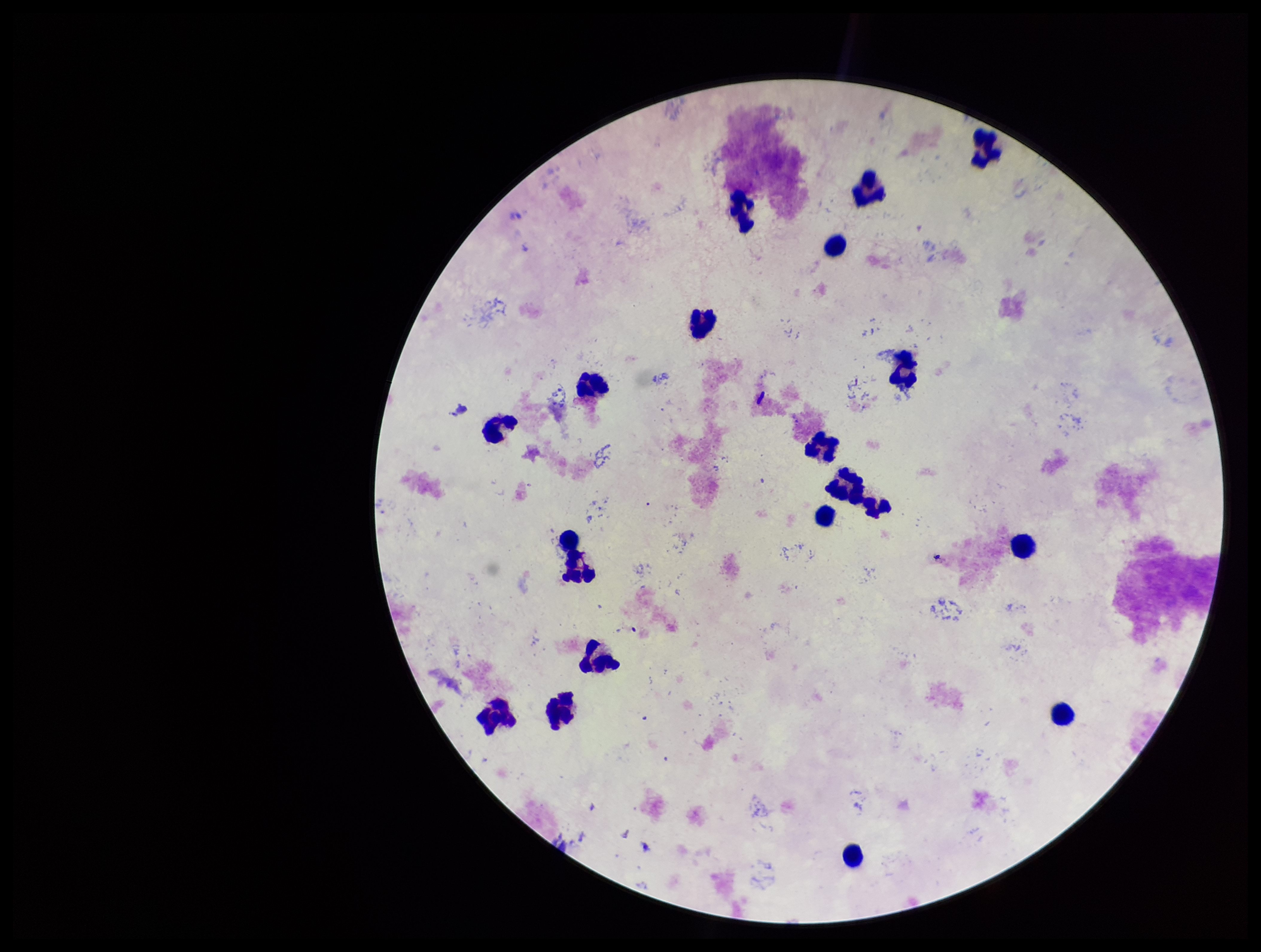 Patient malaria status: negative. Giemsa stain. Photographed through the microscope eyepiece with a smartphone camera. Plasmodium parasites: none identified. Single field of view. Leukocyte count: 19. Parasite count: 0. Preparation: thick smear. Image is 1261×952 pixels.